Classify this cell by malaria status.
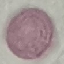
Uninfected.

Summary:
  - Image type: automatically extracted cell patch, resized to 64 × 64 pixels
  - Stain: Giemsa
  - Capture: smartphone camera at the microscope eyepiece
  - Preparation: thin smear